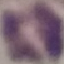

Result: negative for malaria parasites. Giemsa-stained preparation. Automatically extracted cell patch, resized to 64 × 64 pixels. Acquired by smartphone through the microscope eyepiece. Thin blood smear.